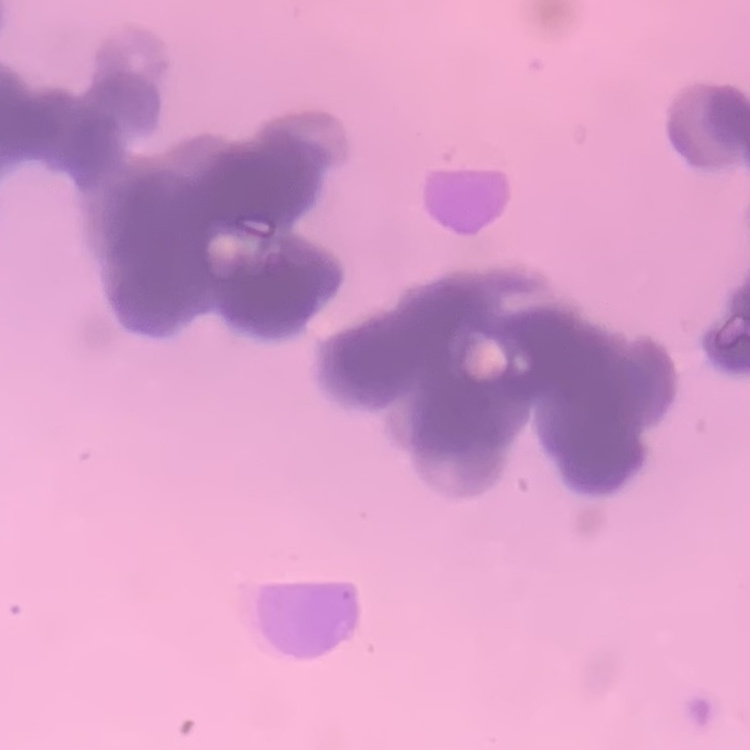 The red blood cells exhibit rouleaux formation. Field's or Giemsa stain. Thin peripheral smear. One tile cut from a larger photomicrograph.